Assess this cell for malaria.
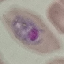

It is parasitized.

Photographed with a smartphone camera at the microscope eyepiece. Thin blood smear. Giemsa-stained preparation. Cell patch, automatically extracted from a larger field of view and resized to 64 × 64 pixels.